Describe the morphology of the red blood cells.
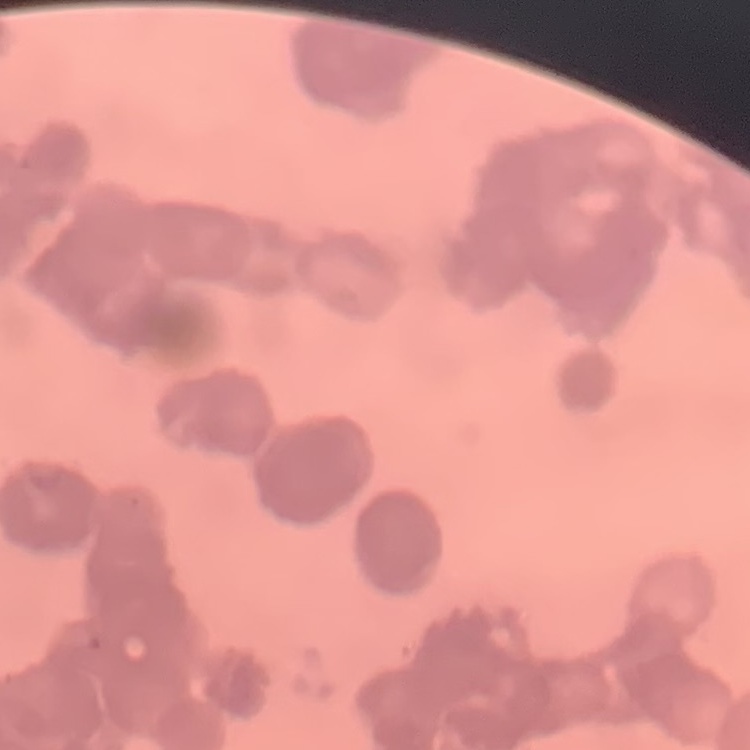
Rouleaux formation.

Summary:
  - Image type: one tile cut from a larger photomicrograph
  - Stain: Field's or Giemsa
  - Preparation: thin blood film